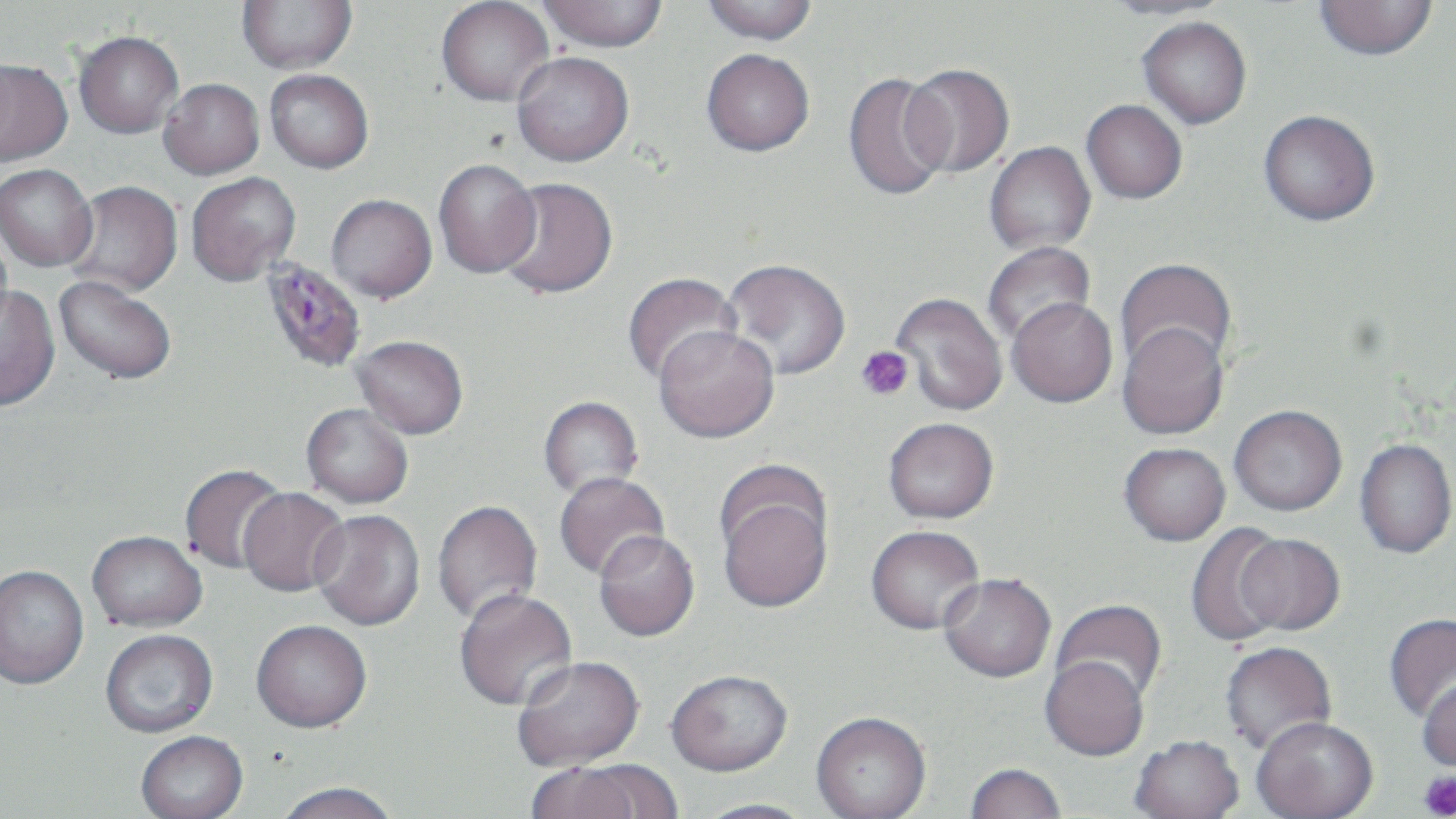

{
  "slide_level_diagnosis": "Plasmodium falciparum",
  "platelet_locations": "approximate bounding boxes as [x1, y1, x2, y2] in pixels: [855, 346, 914, 400], [1420, 771, 1456, 818]",
  "magnification": "1000x",
  "stain": "May-Grünwald-Giemsa",
  "field_of_view": "single",
  "image_size": "1456×819 pixels",
  "plasmodium_falciparum_infected_red_blood_cell_locations": "approximate bounding boxes as [x1, y1, x2, y2] in pixels: [259, 259, 368, 373]",
  "modality": "light microscopy",
  "preparation": "thin blood smear",
  "uninfected_red_blood_cell_locations": "approximate bounding boxes as [x1, y1, x2, y2] in pixels: [237, 0, 356, 74], [436, 0, 554, 106], [537, 0, 668, 53], [700, 0, 818, 45], [1101, 0, 1234, 20], [1314, 0, 1438, 61], [1137, 16, 1252, 129], [74, 30, 183, 138], [701, 48, 815, 156], [511, 51, 634, 166], [0, 58, 72, 166], [901, 63, 1015, 177], [265, 70, 373, 173], [843, 71, 953, 202], [158, 78, 264, 179], [1082, 100, 1187, 203], [1258, 110, 1380, 226], [984, 142, 1095, 255], [433, 159, 541, 279], [0, 164, 97, 271], [186, 172, 300, 285], [495, 177, 618, 299], [63, 181, 183, 297], [326, 194, 437, 302], [982, 242, 1096, 347], [722, 258, 851, 380], [1115, 258, 1237, 374], [621, 272, 740, 385], [54, 275, 177, 384], [0, 285, 60, 412], [891, 292, 1008, 415], [1007, 297, 1118, 407], [1117, 321, 1229, 440], [654, 325, 780, 442], [351, 335, 468, 439], [538, 396, 644, 499], [301, 403, 413, 508], [1229, 405, 1347, 516], [883, 417, 999, 523], [1355, 438, 1456, 559], [1119, 442, 1230, 546], [179, 463, 289, 574], [554, 471, 670, 580], [715, 479, 834, 615], [238, 487, 349, 598], [431, 499, 542, 626], [309, 509, 425, 631], [1185, 522, 1291, 647], [866, 525, 986, 634], [593, 530, 700, 641], [87, 531, 207, 632], [1236, 533, 1345, 635], [0, 565, 89, 690], [938, 573, 1056, 682], [454, 588, 578, 711], [1052, 599, 1168, 705], [1383, 612, 1456, 723], [251, 621, 372, 735], [100, 630, 218, 739], [1220, 641, 1337, 754], [513, 656, 644, 772], [1040, 656, 1150, 761], [666, 670, 793, 777], [1417, 675, 1456, 773], [810, 713, 932, 819], [1252, 716, 1379, 819], [136, 732, 248, 819], [1129, 735, 1245, 819], [524, 762, 653, 819], [964, 763, 1067, 819], [272, 782, 403, 819], [690, 798, 820, 819]"
}